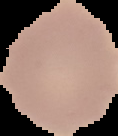
{
  "result": "no malaria parasites detected",
  "preparation": "thin blood film",
  "image_size": "118×136 pixels",
  "image_type": "segmented cell region on a black background"
}